Outline each Trypanosoma brucei.
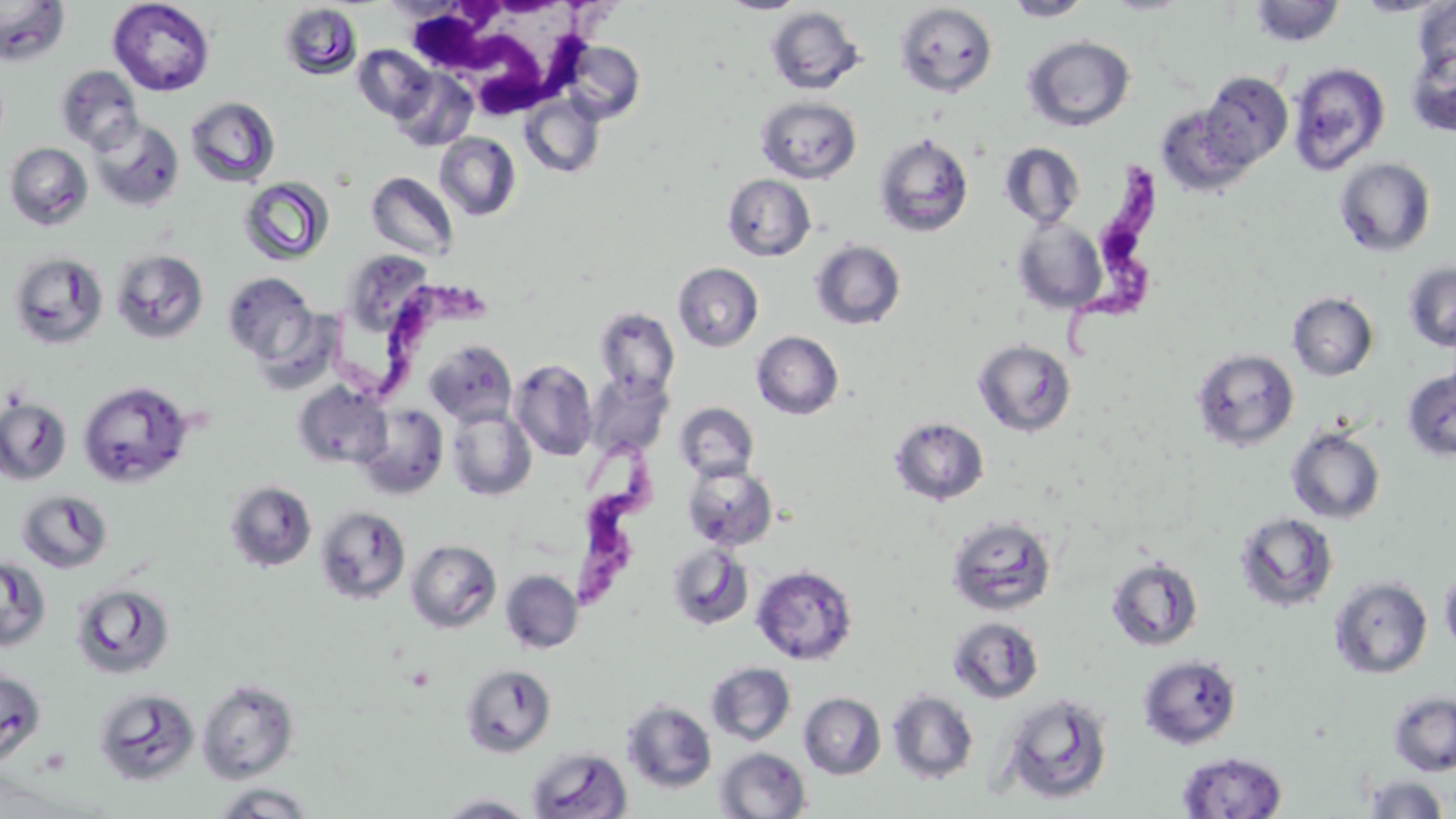

Approximate bounding boxes as (x1, y1, x2, y2) in pixels.
Trypanosoma brucei: (1058, 160, 1165, 367), (324, 271, 487, 404), (560, 430, 662, 608).

White blood cell locations: (402, 2, 588, 115). Uninfected red blood cell locations: (0, 0, 69, 68), (108, 0, 215, 96), (719, 0, 807, 15), (1102, 0, 1192, 15), (1353, 0, 1452, 17), (1005, 1, 1093, 21), (1248, 1, 1346, 47), (1414, 2, 1456, 78), (279, 3, 363, 80), (894, 3, 998, 98), (766, 6, 865, 95), (1023, 35, 1135, 132), (559, 40, 646, 124), (352, 44, 436, 123), (1404, 46, 1456, 137), (1287, 62, 1391, 176), (55, 65, 144, 154), (391, 68, 478, 152), (1199, 70, 1293, 171), (519, 94, 605, 178), (185, 95, 281, 187), (756, 96, 862, 183), (1155, 103, 1255, 196), (88, 117, 184, 212), (873, 131, 974, 237), (434, 132, 521, 221), (3, 142, 93, 231), (999, 142, 1085, 228), (1334, 157, 1436, 258), (366, 171, 459, 262), (722, 173, 816, 261), (239, 176, 334, 266), (1012, 217, 1107, 315), (810, 240, 906, 330), (110, 249, 209, 343), (8, 251, 109, 350), (673, 262, 763, 352), (1403, 262, 1456, 352), (221, 271, 317, 364), (1287, 292, 1378, 381), (595, 307, 679, 398), (751, 331, 844, 419), (973, 339, 1076, 438), (424, 340, 517, 426), (1191, 348, 1300, 452), (510, 360, 598, 460), (1402, 369, 1456, 463), (585, 372, 674, 456), (78, 381, 194, 488), (292, 382, 391, 470), (0, 397, 71, 485), (675, 402, 759, 481), (357, 404, 449, 500), (446, 407, 536, 501), (889, 416, 990, 506), (1285, 426, 1386, 524), (681, 462, 778, 550), (224, 480, 317, 572), (16, 489, 114, 573), (315, 506, 411, 605), (1233, 511, 1339, 613), (946, 515, 1058, 616), (406, 540, 501, 633), (667, 542, 754, 630), (1105, 556, 1203, 651), (1, 557, 52, 652), (751, 565, 858, 665), (1440, 567, 1456, 657), (500, 570, 583, 653), (1329, 576, 1433, 679), (70, 581, 175, 680), (947, 616, 1044, 704), (1139, 655, 1242, 749), (705, 661, 796, 746), (460, 663, 557, 757), (0, 669, 46, 765), (197, 679, 299, 783), (93, 687, 201, 785), (887, 690, 978, 784), (999, 690, 1115, 804), (1388, 691, 1456, 776), (799, 692, 886, 779), (622, 700, 717, 793), (527, 747, 632, 819), (715, 747, 811, 819), (1177, 751, 1287, 818), (1363, 775, 1450, 818), (210, 782, 318, 817), (434, 794, 540, 818). Slide-level diagnosis: Trypanosoma brucei. Light microscopy. Image is 1456×819 pixels. 1000x magnification. Thin blood smear. One field of a larger specimen. May-Grünwald-Giemsa-stained preparation.